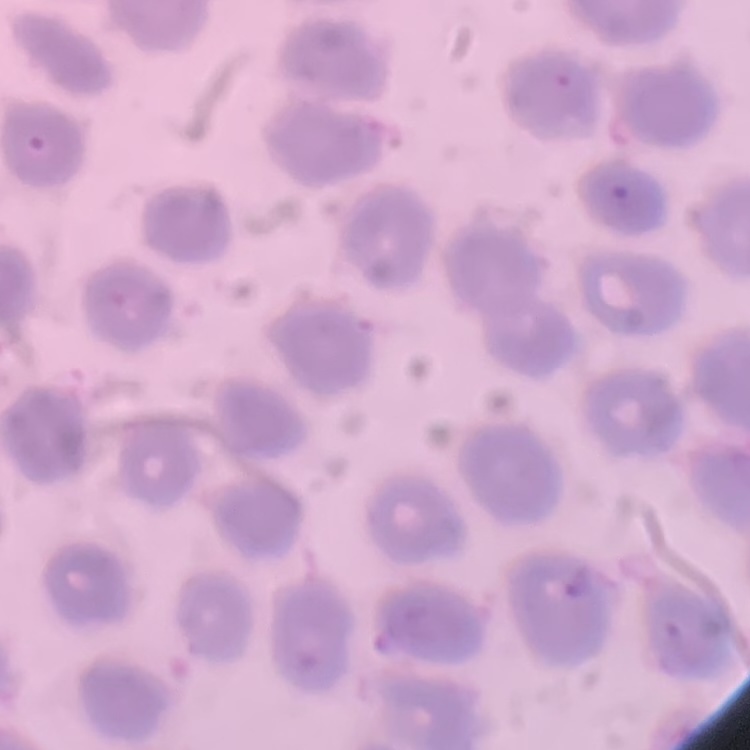
Summary:
  - Red blood cell morphology: no rouleaux formation
  - Image type: square crop of a larger photomicrograph
  - Stain: Field's or Giemsa
  - Preparation: thin blood smear